Classify this cell by malaria status.
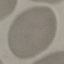
Uninfected.

Photographed with a smartphone camera at the microscope eyepiece. Thin smear of blood. Automatically extracted cell patch, resized to 64 × 64 pixels. Giemsa-stained preparation.